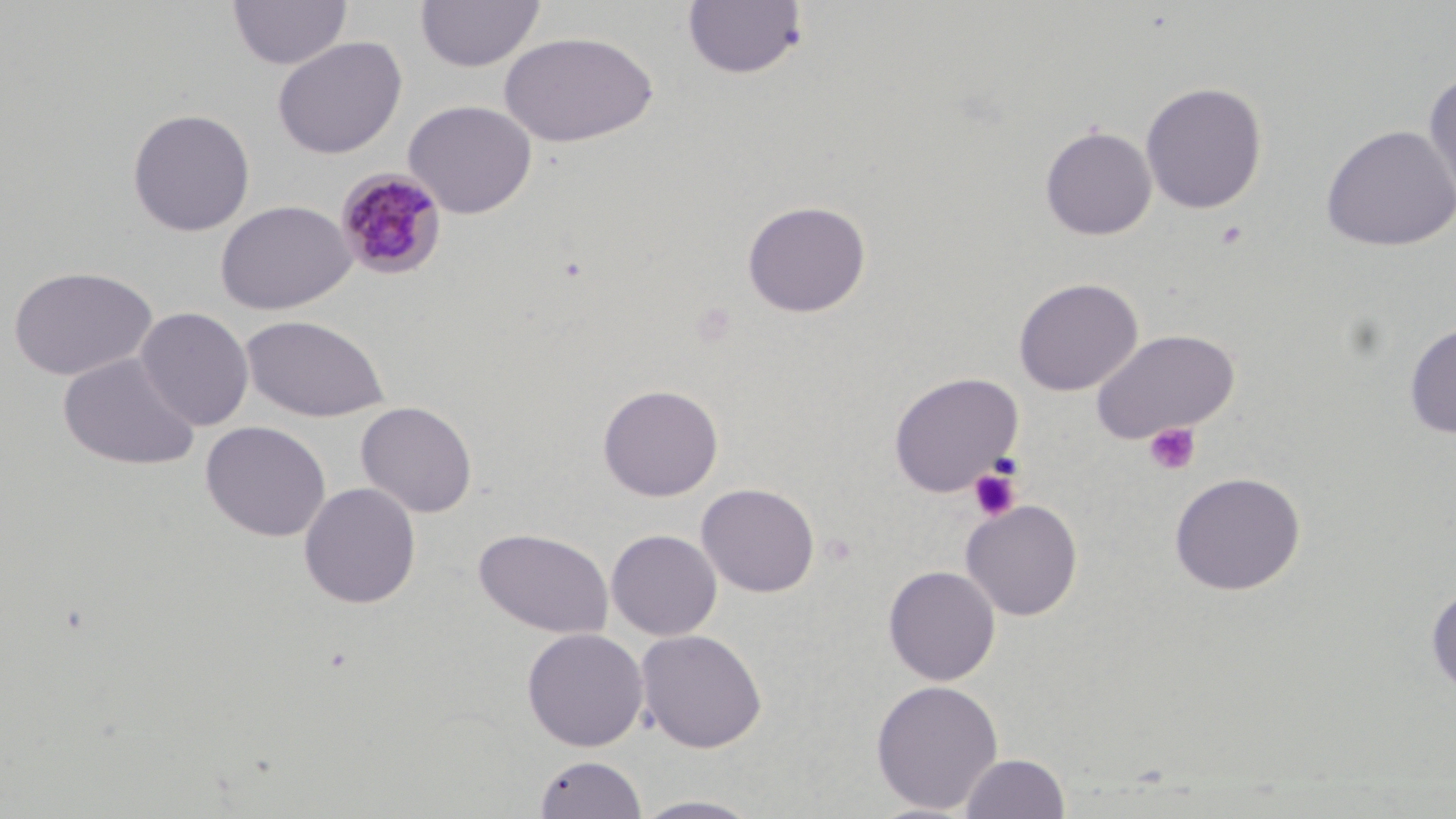
Summary:
  - Coordinate format: approximate bounding boxes as named x1/y1/x2/y2 corners in pixels
  - Platelet locations: (x1=1143, y1=422, x2=1202, y2=476), (x1=966, y1=466, x2=1022, y2=522)
  - Plasmodium malariae-infected red blood cell locations (subset): (x1=335, y1=168, x2=449, y2=281)
  - Uninfected red blood cell locations (subset): (x1=228, y1=0, x2=352, y2=70), (x1=415, y1=0, x2=546, y2=73), (x1=683, y1=1, x2=808, y2=81), (x1=499, y1=30, x2=658, y2=147), (x1=272, y1=36, x2=408, y2=160), (x1=1423, y1=71, x2=1456, y2=209), (x1=1140, y1=81, x2=1268, y2=215), (x1=402, y1=98, x2=538, y2=218), (x1=127, y1=108, x2=255, y2=237), (x1=1320, y1=124, x2=1456, y2=252), (x1=1039, y1=125, x2=1157, y2=240), (x1=741, y1=199, x2=871, y2=318), (x1=7, y1=265, x2=157, y2=380), (x1=1013, y1=277, x2=1142, y2=396), (x1=135, y1=306, x2=255, y2=431), (x1=240, y1=313, x2=390, y2=422), (x1=1404, y1=322, x2=1456, y2=438), (x1=1090, y1=328, x2=1240, y2=444), (x1=57, y1=352, x2=200, y2=472), (x1=888, y1=372, x2=1024, y2=498), (x1=597, y1=383, x2=723, y2=502), (x1=356, y1=401, x2=478, y2=518), (x1=200, y1=420, x2=331, y2=542), (x1=1169, y1=471, x2=1306, y2=596), (x1=298, y1=482, x2=421, y2=609), (x1=696, y1=482, x2=820, y2=598), (x1=961, y1=499, x2=1083, y2=620), (x1=474, y1=527, x2=613, y2=639), (x1=606, y1=528, x2=722, y2=640), (x1=883, y1=565, x2=1001, y2=685), (x1=1426, y1=585, x2=1456, y2=696), (x1=521, y1=627, x2=649, y2=751), (x1=636, y1=629, x2=768, y2=752), (x1=870, y1=678, x2=1004, y2=814), (x1=960, y1=752, x2=1070, y2=818), (x1=533, y1=754, x2=648, y2=818), (x1=631, y1=794, x2=767, y2=818)
  - Slide-level diagnosis: Plasmodium malariae
  - Magnification: 1000x
  - Image size: 1456×819 pixels
  - Preparation: thin blood smear
  - Modality: optical microscopy
  - Stain: May-Grünwald-Giemsa
  - Field of view: one of a larger specimen